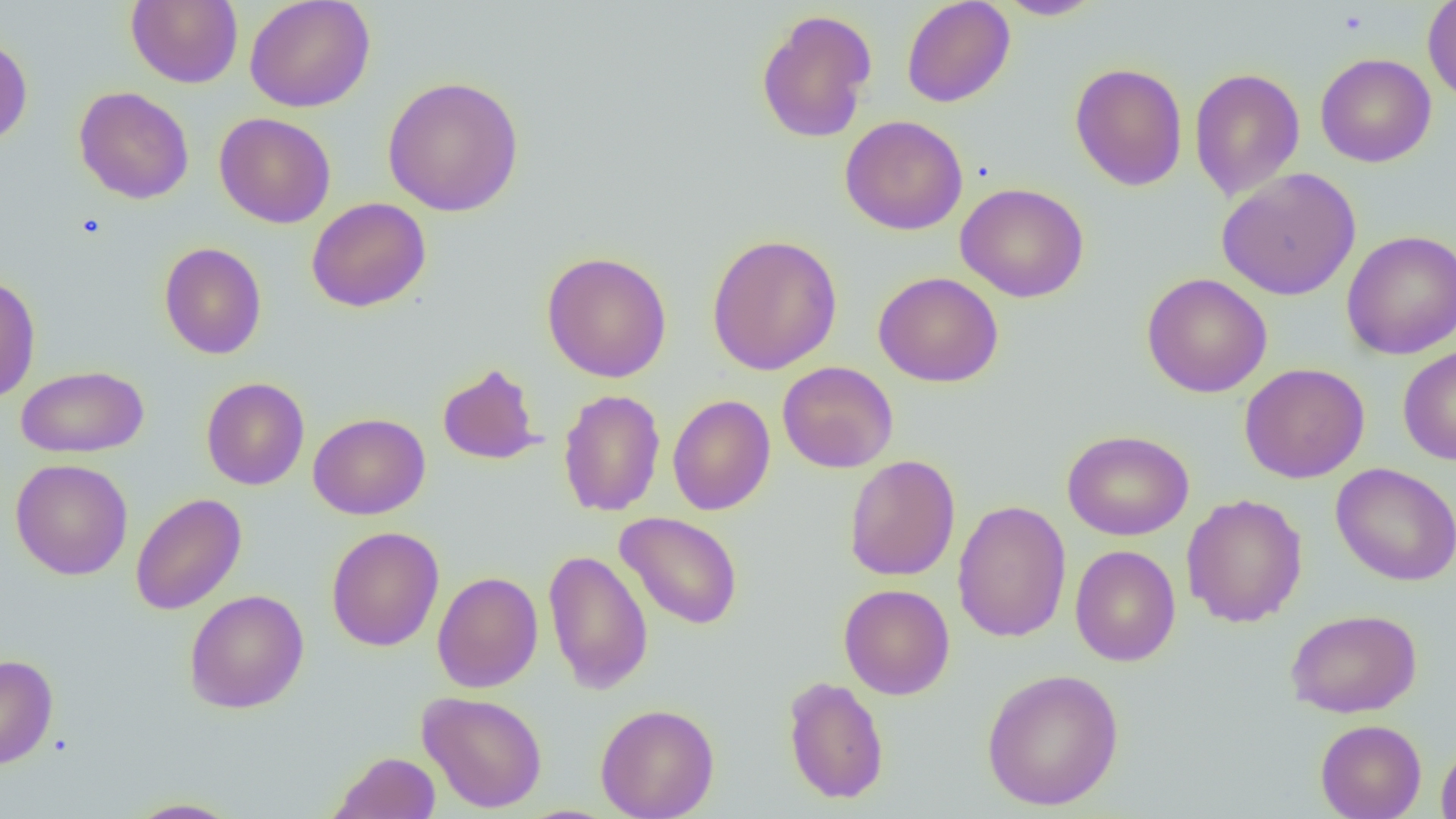
Approximate bounding boxes as named x1/y1/x2/y2 corners in pixels. Uninfected red blood cell locations: (x1=126, y1=0, x2=244, y2=89), (x1=244, y1=0, x2=376, y2=113), (x1=901, y1=0, x2=1015, y2=108), (x1=994, y1=0, x2=1104, y2=20), (x1=1422, y1=0, x2=1456, y2=103), (x1=755, y1=8, x2=877, y2=144), (x1=0, y1=33, x2=33, y2=147), (x1=1315, y1=52, x2=1436, y2=168), (x1=1069, y1=62, x2=1188, y2=191), (x1=1189, y1=67, x2=1305, y2=201), (x1=382, y1=76, x2=525, y2=217), (x1=74, y1=86, x2=194, y2=204), (x1=214, y1=112, x2=336, y2=229), (x1=840, y1=115, x2=968, y2=235), (x1=1216, y1=167, x2=1361, y2=300), (x1=955, y1=182, x2=1089, y2=303), (x1=306, y1=197, x2=431, y2=313), (x1=1341, y1=229, x2=1456, y2=360), (x1=706, y1=233, x2=843, y2=376), (x1=159, y1=242, x2=267, y2=359), (x1=541, y1=251, x2=673, y2=383), (x1=874, y1=271, x2=1004, y2=387), (x1=0, y1=273, x2=41, y2=404), (x1=1141, y1=273, x2=1272, y2=398), (x1=1397, y1=345, x2=1456, y2=466), (x1=777, y1=361, x2=899, y2=473), (x1=436, y1=362, x2=544, y2=465), (x1=1240, y1=362, x2=1369, y2=483), (x1=16, y1=365, x2=149, y2=458), (x1=200, y1=376, x2=310, y2=490), (x1=558, y1=389, x2=666, y2=517), (x1=667, y1=394, x2=775, y2=515), (x1=308, y1=412, x2=430, y2=519), (x1=1062, y1=430, x2=1194, y2=541), (x1=843, y1=454, x2=960, y2=581), (x1=11, y1=459, x2=133, y2=580), (x1=1330, y1=463, x2=1456, y2=586), (x1=130, y1=492, x2=246, y2=615), (x1=1181, y1=494, x2=1308, y2=628), (x1=952, y1=499, x2=1071, y2=643), (x1=615, y1=511, x2=744, y2=630), (x1=326, y1=526, x2=444, y2=651), (x1=1069, y1=544, x2=1181, y2=667), (x1=543, y1=548, x2=653, y2=695), (x1=431, y1=571, x2=543, y2=693), (x1=839, y1=583, x2=955, y2=700), (x1=184, y1=589, x2=309, y2=713), (x1=1285, y1=608, x2=1422, y2=718), (x1=0, y1=654, x2=58, y2=770), (x1=981, y1=668, x2=1124, y2=811), (x1=782, y1=675, x2=889, y2=804), (x1=417, y1=690, x2=548, y2=813), (x1=595, y1=702, x2=720, y2=819), (x1=1315, y1=719, x2=1427, y2=819), (x1=1436, y1=741, x2=1456, y2=819), (x1=328, y1=751, x2=441, y2=818), (x1=125, y1=797, x2=246, y2=818). Slide-level diagnosis: negative for blood parasites. Image is 1456×819 pixels. 1000x magnification. One field of a larger specimen. Thin blood film. Light microscopy.